Assess this cell for malaria.
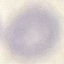
Uninfected.

Automatically extracted cell patch, resized to 64 × 64 pixels. Acquired by smartphone through the microscope eyepiece. Thin blood smear. Giemsa stain.